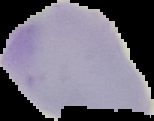
Summary:
  - Image type: segmented cell region on a black background
  - Preparation: thin blood film
  - Image size: 154×121 pixels
  - Malaria status: uninfected